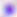

Summary:
  - Magnification: 400x
  - Modality: micrograph
  - Identification: Toxoplasma gondii